Report the malaria status of this cell.
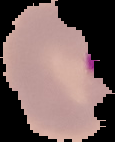
It is parasitized.

Summary:
  - Image size: 115×142 pixels
  - Image type: segmented cell region with the area outside set to black
  - Preparation: thin blood smear